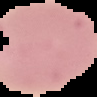

Malaria status: parasitized. Cell region segmented out of the field of view; the surrounding area is masked to black. From a thin blood film. Image is 97×97 pixels.